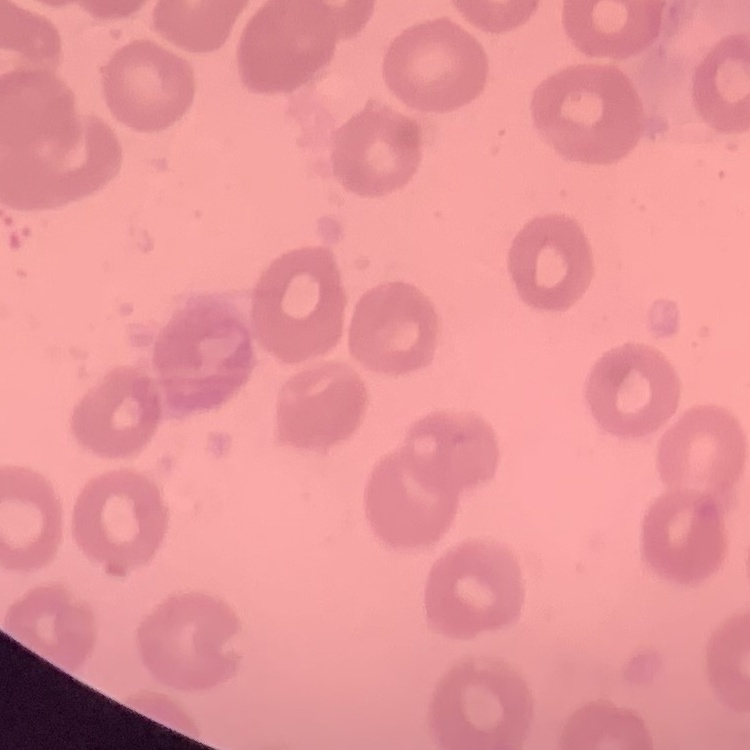
The red blood cells exhibit no rouleaux formation. Stained with either Field's or Giemsa. One tile cut from a larger photomicrograph. Thin blood smear.